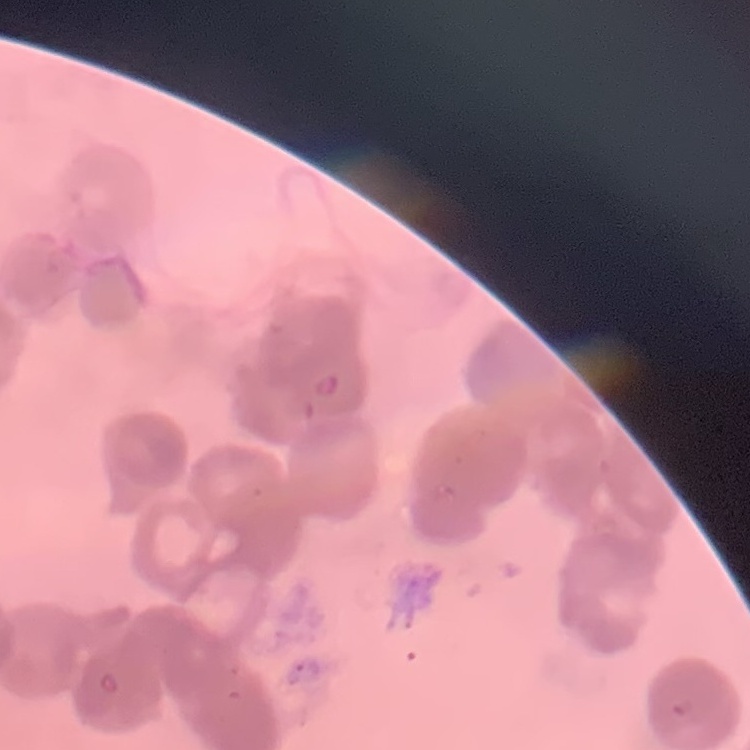

The erythrocytes exhibit rouleaux formation. Stained with either Field's or Giemsa. Thin blood film. Square crop of a larger photomicrograph.